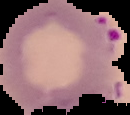

Summary:
  - Image type: segmented cell region with the area outside set to black
  - Result: malaria parasites identified
  - Image size: 130×115 pixels
  - Preparation: thin blood smear